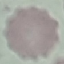
result = no malaria parasites detected
capture = smartphone camera at the microscope eyepiece
stain = Giemsa
image type = cell patch, automatically extracted from a larger field of view and resized to 64 × 64 pixels
preparation = thin blood film